Classify this cell by malaria status.
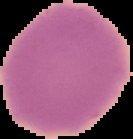

Uninfected.

{
  "image_type": "cell region segmented out of the field of view; surrounding area masked to black",
  "image_size": "133×139 pixels",
  "preparation": "thin blood film"
}